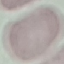 Result: no malaria parasites seen. Acquired by smartphone through the microscope eyepiece. Giemsa-stained preparation. Automatically extracted cell patch, resized to 64 × 64 pixels. Thin smear of blood.